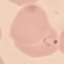 Malaria status: parasitized. Cell patch, automatically extracted from a larger field of view and resized to 64 × 64 pixels. Photographed with a smartphone camera at the microscope eyepiece. Thin blood smear. Giemsa-stained preparation.